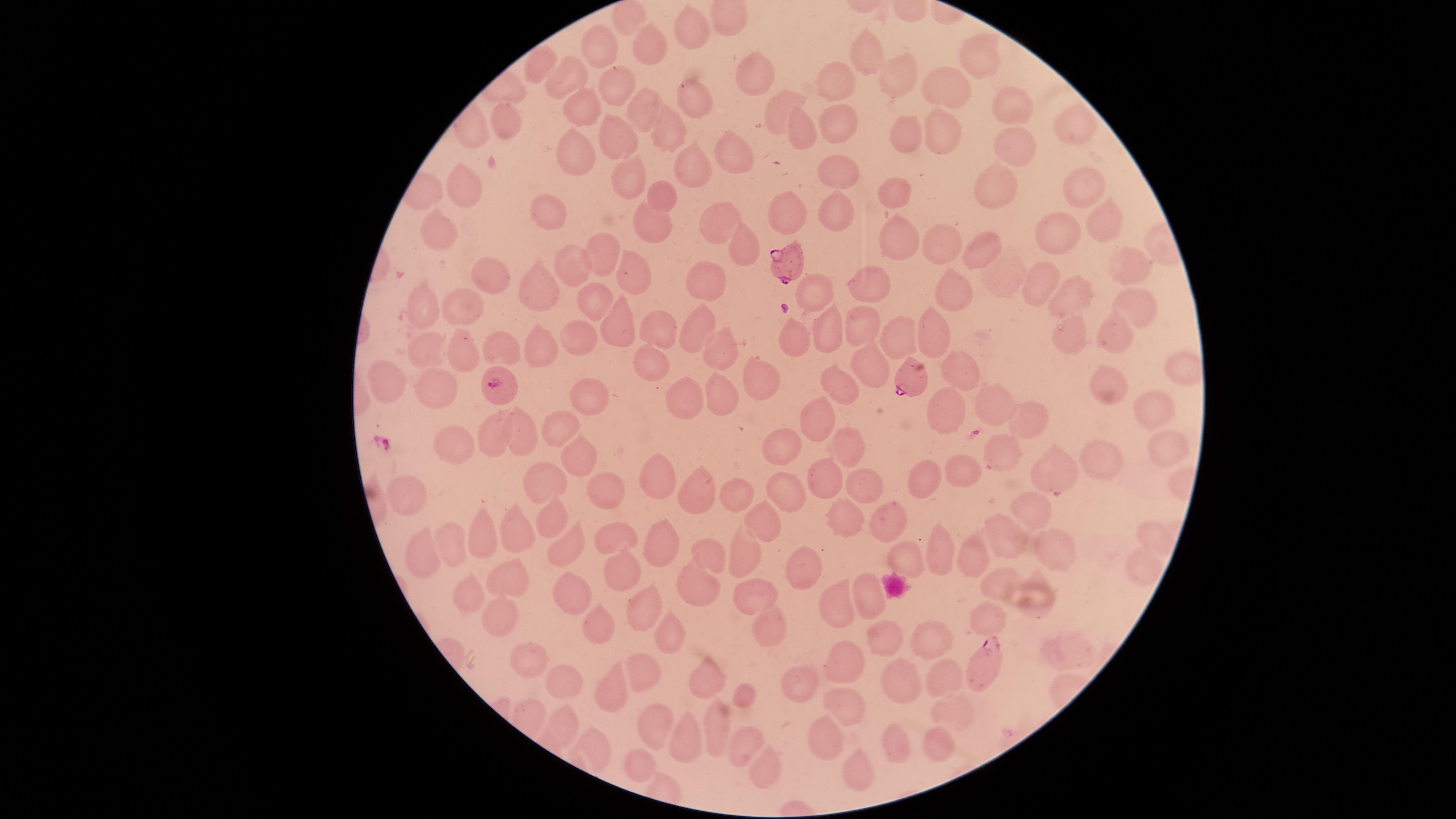

preparation = thin blood film
presence = malaria parasites identified
visible region = circular
capture = smartphone photograph through the microscope eyepiece
uninfected red blood cells = approximate marker points as [x, y] in pixels: [628, 20], [691, 26], [649, 49], [606, 50], [867, 52], [972, 59], [539, 64], [756, 72], [572, 75], [834, 78], [899, 81], [613, 85], [950, 88], [691, 94], [580, 109], [636, 111], [777, 111], [1010, 111], [1074, 124], [504, 125], [833, 125], [672, 127], [799, 129], [909, 131], [932, 133], [611, 139], [1018, 150], [734, 151], [577, 157], [693, 163], [834, 174], [630, 176], [1084, 183], [468, 184], [891, 186], [992, 190], [663, 193], [833, 212], [783, 215], [1101, 220], [653, 223], [722, 224], [548, 226], [441, 231], [893, 232], [1063, 237], [947, 244], [991, 248], [746, 251], [601, 253], [1124, 261], [630, 268], [570, 272], [482, 274], [873, 277], [710, 278], [1004, 282], [1043, 284], [963, 286], [538, 289], [816, 289], [596, 300], [1072, 302], [1132, 305], [423, 307], [467, 312], [619, 321], [863, 323], [696, 324], [662, 328], [825, 329], [938, 333], [1113, 333], [891, 334], [791, 335], [1076, 339], [583, 343], [545, 345], [462, 346], [428, 347], [503, 350], [718, 351], [652, 360], [872, 367], [963, 376], [754, 377], [837, 382], [390, 384], [594, 389], [1103, 390], [437, 394], [682, 396], [722, 399], [999, 401], [946, 409], [1154, 413], [812, 415], [1028, 417], [559, 426], [496, 435], [519, 435], [846, 442], [1153, 443], [455, 448], [1004, 448], [782, 449], [582, 450], [1092, 465], [962, 468], [1054, 471], [826, 477], [546, 480], [664, 481], [924, 482], [857, 485], [603, 490], [789, 493], [736, 495], [407, 496], [696, 496], [1034, 510], [760, 518], [556, 519], [891, 520], [846, 523], [514, 533], [616, 533], [1151, 535], [1008, 538], [484, 542], [661, 542], [1050, 545], [452, 546], [570, 547], [938, 552], [967, 552], [698, 554], [424, 555], [745, 557], [909, 557], [797, 564], [623, 568], [1140, 572], [499, 579], [698, 582], [999, 584], [753, 594], [470, 595], [571, 595], [1033, 597], [869, 598], [838, 600], [644, 609], [496, 612], [992, 620], [593, 622], [765, 625], [670, 632], [885, 640], [930, 640], [1060, 652], [525, 659], [842, 669], [645, 672], [941, 672], [704, 676], [898, 682], [562, 683], [804, 686], [606, 690], [747, 694], [844, 709], [950, 712], [716, 722], [565, 725], [656, 733], [828, 739], [892, 741], [940, 741], [688, 742], [736, 743], [597, 750], [762, 762], [636, 764], [857, 770]
field of view = single
parasitized red blood cells = approximate marker points as [x, y] in pixels: [789, 265], [914, 377], [497, 386], [985, 664]
species = Plasmodium falciparum
image size = 1456×819 pixels
stain = Giemsa